Report the malaria status of this cell.
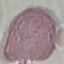
It is uninfected.

Giemsa stain. Automatically extracted cell patch, resized to 64 × 64 pixels. Acquired by smartphone through the microscope eyepiece. Thin blood smear.